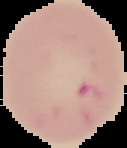

Summary:
  - Preparation: thin blood smear
  - Result: Plasmodium parasites detected
  - Image size: 127×148 pixels
  - Image type: segmented cell region with the area outside set to black